Assess the morphology of the erythrocytes.
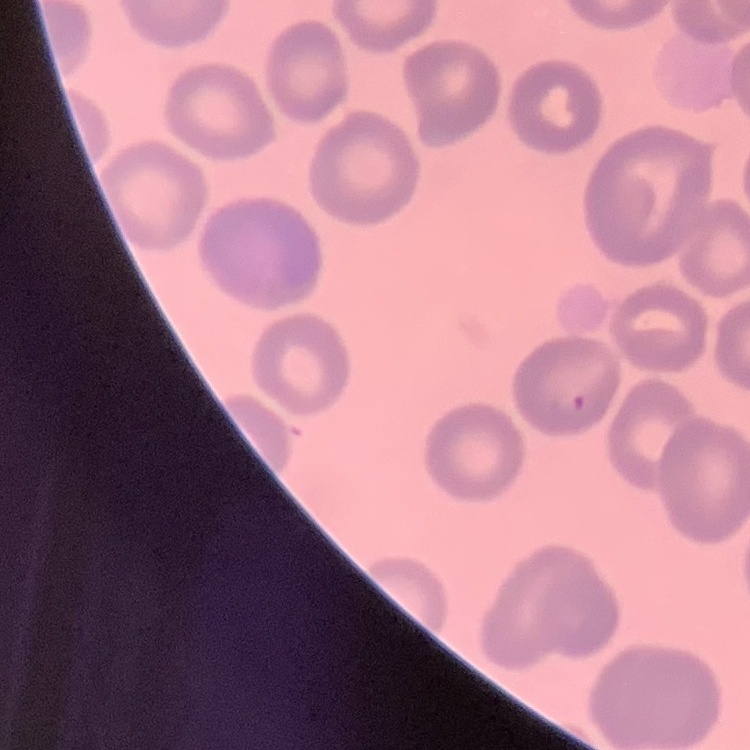
No rouleaux formation.

Field's or Giemsa stain. Thin peripheral smear. One tile cut from a larger photomicrograph.